Look for Plasmodium parasites.
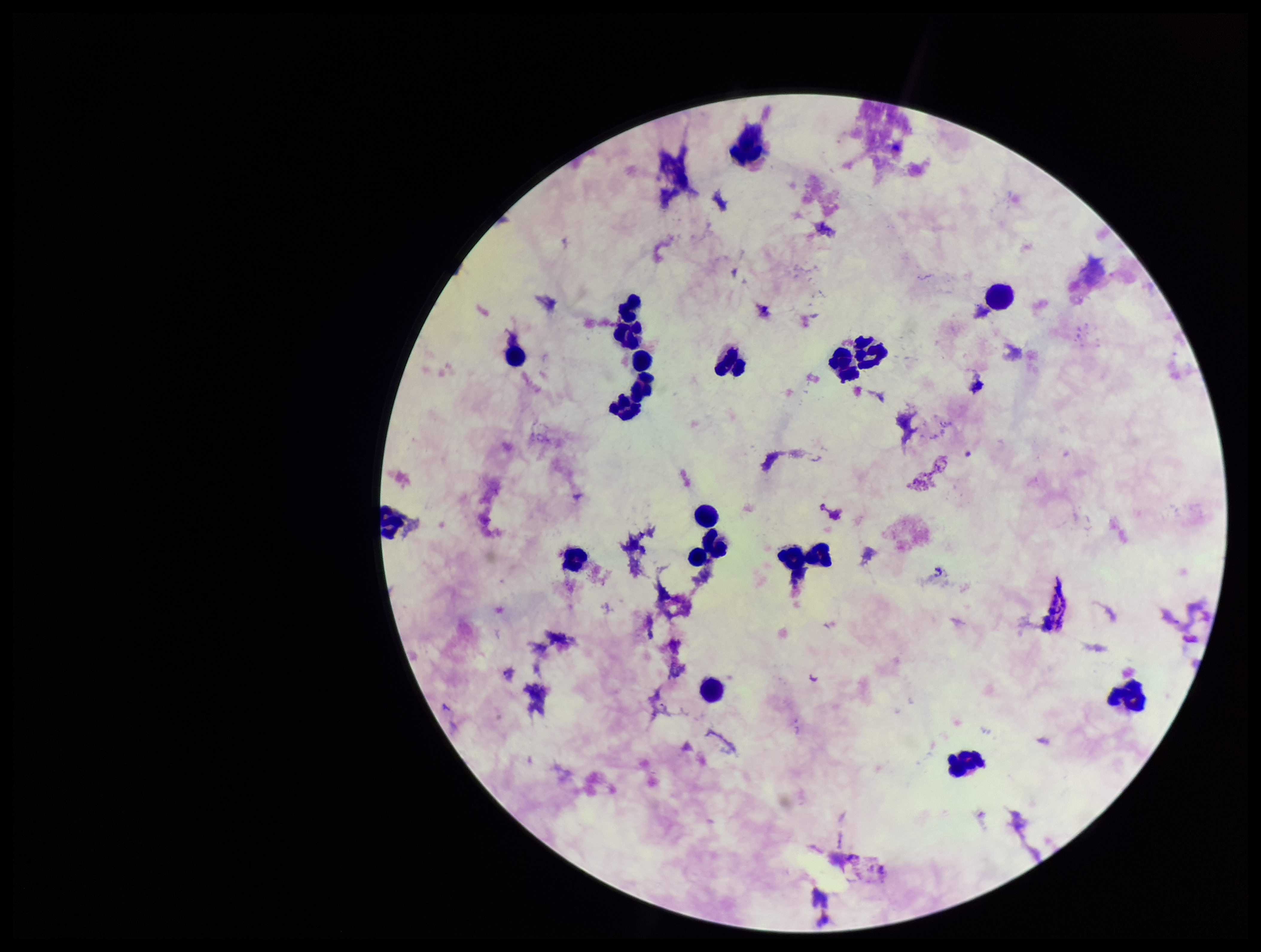

None seen.

Giemsa stain. Image is 1261×952 pixels. Leukocyte count: 21. Smartphone photograph taken through the eyepiece of a microscope. Parasite count: 0. Single field of view. Patient malaria status: negative. Preparation: thick.